Assess this cell for malaria.
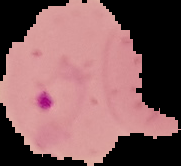
Parasitized.

Segmented cell region on a black background. From a thin blood smear. Image is 181×166 pixels.